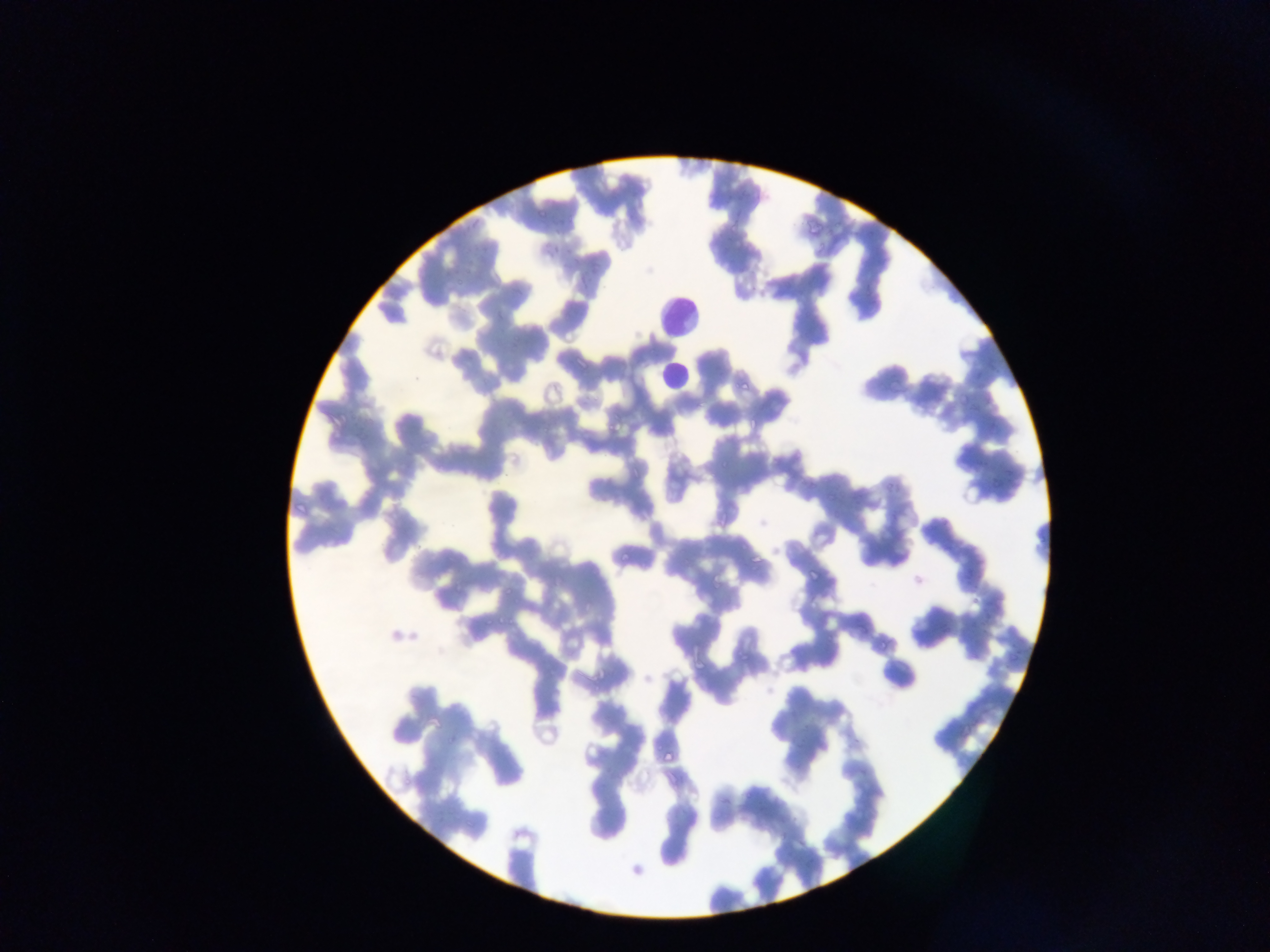

Approximate bounding boxes as left top right bottom in pixels. Malaria parasite locations: 539 208 545 216; 536 249 546 264; 574 273 587 291; 512 338 518 352; 739 377 756 392; 747 416 761 431; 606 424 623 435; 715 509 730 528; 748 552 759 564; 619 555 629 563; 810 571 818 580; 450 578 463 596; 503 586 511 593; 496 614 504 628; 663 745 677 762; 511 871 521 881. Leukocyte locations: 653 293 706 346; 653 355 684 398. Mobile-phone photograph taken through the microscope. Thin blood smear. Sample from Ghana. One field of view. Image is 1270×952 pixels.